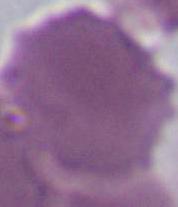 A red blood cell is shown. Micrograph. 1000x magnification.